Assess for Plasmodium parasites.
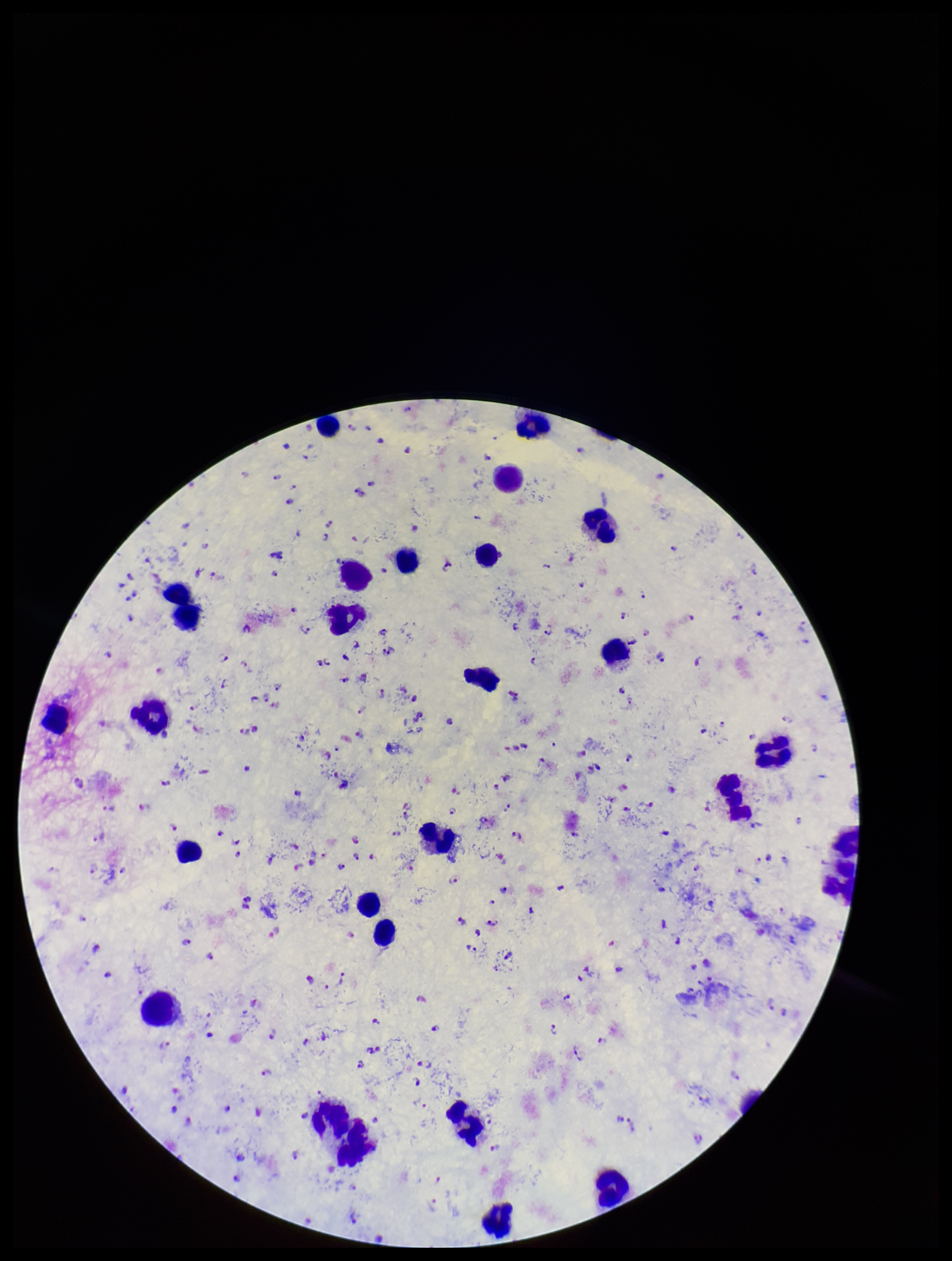

Identified.

Single field of view. Giemsa stain. Leukocyte count: 30. Image is 952×1261 pixels. Parasite count: 222. Patient malaria status: infected. Photographed through the microscope eyepiece with a smartphone camera. Preparation: thick smear. Species reported for this patient: Plasmodium falciparum.